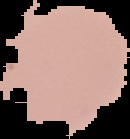 Image is 130×139 pixels. Segmented cell region on a black background. From a thin blood smear. Malaria status: uninfected.